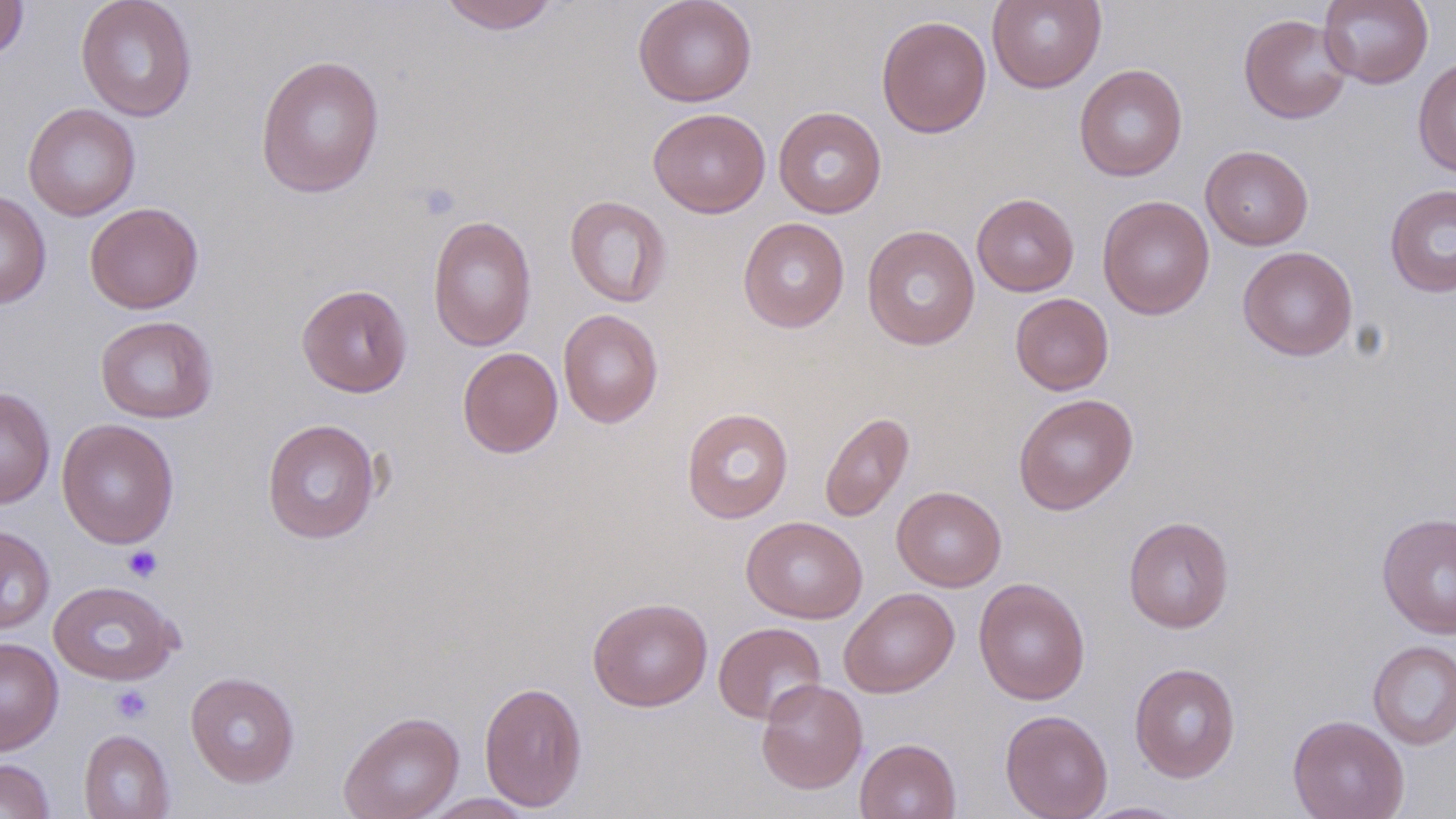

slide-level diagnosis = no evidence of blood parasites
platelet locations = approximate bounding boxes as (x1, y1, x2, y2) in pixels: (123, 546, 163, 582), (111, 685, 152, 723)
uninfected red blood cell locations = approximate bounding boxes as (x1, y1, x2, y2) in pixels: (75, 0, 198, 122), (633, 0, 757, 107), (987, 0, 1106, 93), (1318, 0, 1433, 88), (0, 1, 30, 63), (438, 1, 561, 34), (1238, 13, 1353, 124), (876, 14, 992, 139), (254, 54, 386, 198), (1412, 57, 1456, 178), (1074, 64, 1188, 182), (22, 103, 140, 221), (773, 106, 887, 218), (648, 108, 771, 218), (1200, 145, 1314, 250), (1384, 183, 1456, 298), (0, 190, 51, 308), (972, 193, 1079, 297), (565, 195, 672, 308), (1097, 195, 1214, 320), (85, 202, 203, 314), (427, 214, 537, 353), (737, 216, 850, 333), (862, 224, 980, 351), (1237, 246, 1358, 361), (296, 284, 413, 397), (1010, 293, 1113, 395), (558, 308, 663, 428), (95, 315, 218, 423), (457, 347, 562, 458), (0, 387, 55, 509), (1013, 393, 1138, 515), (681, 407, 794, 524), (819, 411, 915, 523), (56, 418, 179, 549), (261, 418, 382, 544), (892, 486, 1006, 592), (1376, 512, 1456, 639), (742, 516, 868, 623), (1123, 516, 1234, 633), (0, 525, 55, 635), (974, 577, 1091, 705), (48, 580, 181, 685), (839, 587, 960, 698), (587, 596, 713, 712), (713, 622, 826, 725), (0, 637, 63, 755), (1367, 640, 1456, 750), (1129, 662, 1241, 783), (185, 671, 300, 787), (755, 678, 868, 794), (478, 681, 588, 812), (999, 709, 1113, 819), (338, 711, 465, 819), (1288, 714, 1410, 819), (78, 729, 175, 819), (855, 738, 961, 818), (0, 758, 55, 819), (418, 793, 539, 818), (1077, 801, 1192, 818)
stain = May-Grünwald-Giemsa
field of view = one of a larger specimen
modality = light microscopy
magnification = 1000x
preparation = thin blood smear
image size = 1456×819 pixels